Describe the morphology of the erythrocytes.
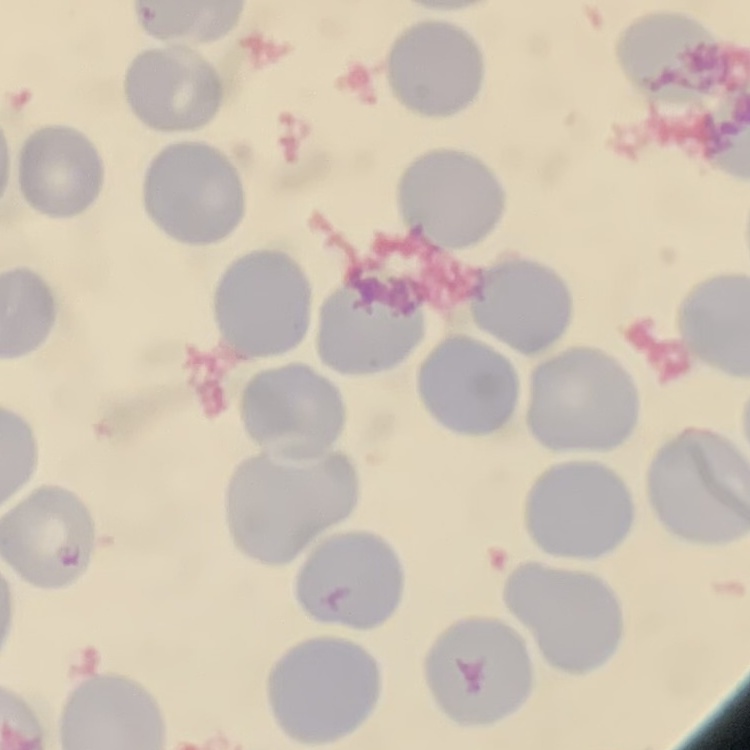
They show no rouleaux formation.

{
  "image_type": "square crop of a larger photomicrograph",
  "preparation": "thin blood film",
  "stain": "Field's or Giemsa"
}